Describe the morphology of the erythrocytes.
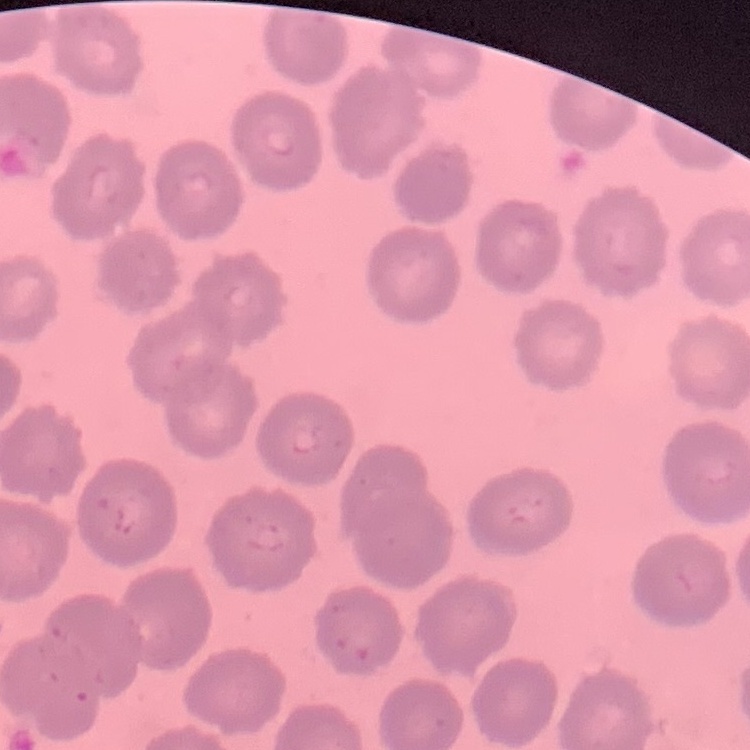
No rouleaux formation.

{
  "image_type": "square crop of a larger photomicrograph",
  "stain": "Field's or Giemsa",
  "preparation": "thin blood film"
}